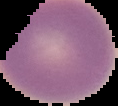

From a thin blood film. Result: no Plasmodium parasites seen. Image is 118×106 pixels. Segmented cell region on a black background.